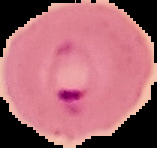
Summary:
  - Image size: 157×148 pixels
  - Malaria status: parasitized
  - Preparation: thin blood film
  - Image type: segmented cell region with the area outside set to black